Report the malaria status of this cell.
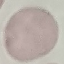

Uninfected.

preparation = thin blood smear
stain = Giemsa
capture = smartphone camera at the microscope eyepiece
image type = automatically extracted cell patch, resized to 64 × 64 pixels